Locate every uninfected red blood cell.
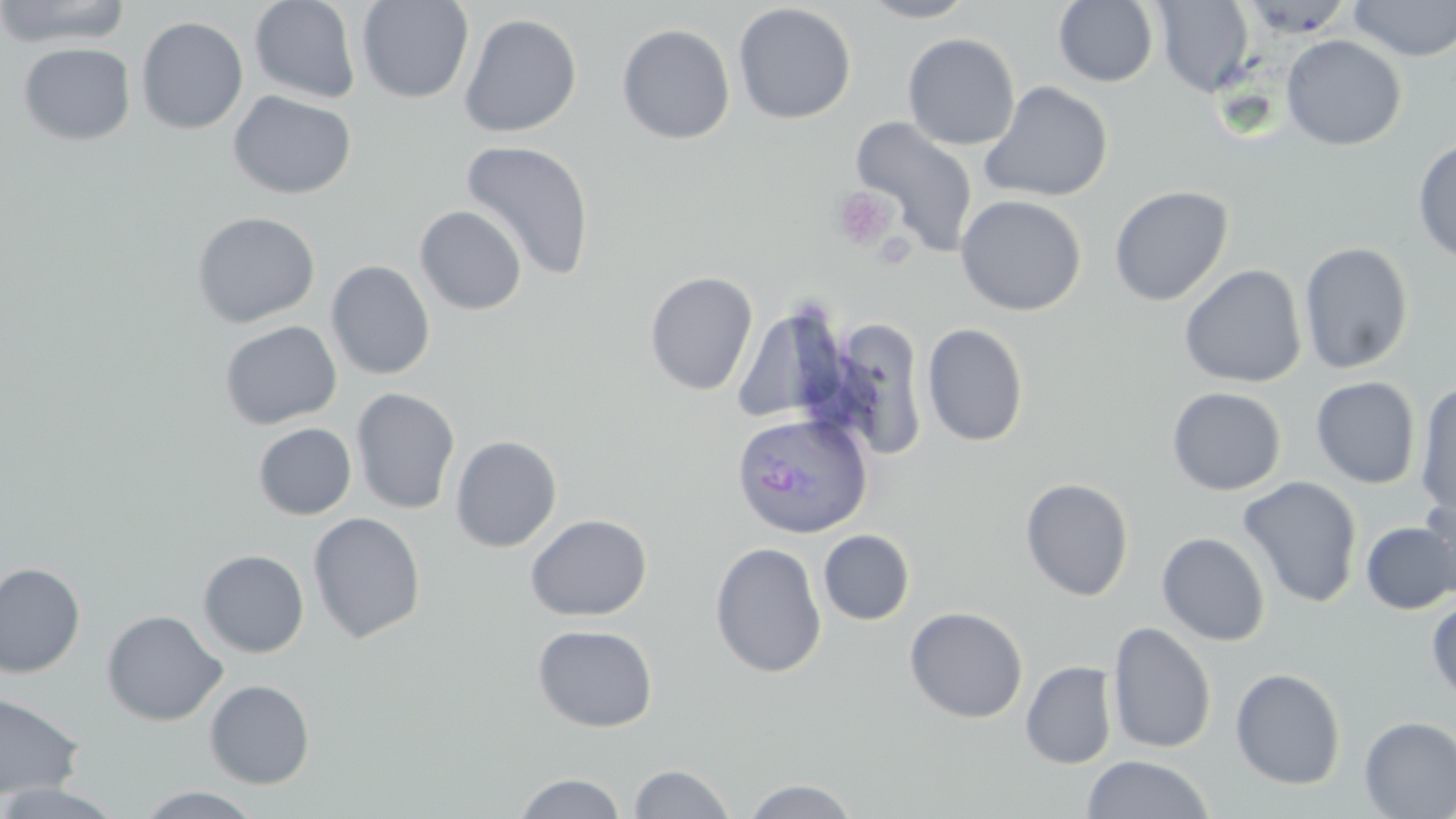
Approximate bounding boxes as named x1/y1/x2/y2 corners in pixels.
Uninfected red blood cells: (x1=0, y1=0, x2=133, y2=48), (x1=249, y1=0, x2=362, y2=104), (x1=356, y1=0, x2=474, y2=104), (x1=858, y1=0, x2=978, y2=23), (x1=1054, y1=0, x2=1159, y2=87), (x1=1348, y1=0, x2=1456, y2=61), (x1=1153, y1=1, x2=1255, y2=97), (x1=733, y1=3, x2=857, y2=124), (x1=458, y1=12, x2=582, y2=138), (x1=136, y1=16, x2=249, y2=135), (x1=616, y1=23, x2=735, y2=144), (x1=902, y1=33, x2=1020, y2=151), (x1=1281, y1=35, x2=1407, y2=151), (x1=18, y1=42, x2=136, y2=146), (x1=980, y1=80, x2=1114, y2=203), (x1=228, y1=90, x2=356, y2=200), (x1=849, y1=116, x2=979, y2=257), (x1=460, y1=139, x2=595, y2=282), (x1=1412, y1=139, x2=1456, y2=264), (x1=1109, y1=185, x2=1233, y2=306), (x1=955, y1=194, x2=1087, y2=316), (x1=414, y1=205, x2=527, y2=316), (x1=191, y1=211, x2=320, y2=328), (x1=1299, y1=242, x2=1414, y2=374), (x1=326, y1=260, x2=436, y2=380), (x1=1179, y1=264, x2=1307, y2=389), (x1=644, y1=271, x2=759, y2=396), (x1=731, y1=300, x2=851, y2=428), (x1=838, y1=316, x2=924, y2=459), (x1=219, y1=320, x2=342, y2=430), (x1=921, y1=322, x2=1029, y2=447), (x1=1311, y1=376, x2=1420, y2=489), (x1=1415, y1=382, x2=1456, y2=519), (x1=350, y1=387, x2=461, y2=515), (x1=1167, y1=387, x2=1286, y2=496), (x1=253, y1=422, x2=357, y2=519), (x1=450, y1=435, x2=562, y2=553), (x1=1238, y1=476, x2=1363, y2=607), (x1=1020, y1=477, x2=1134, y2=601), (x1=1419, y1=491, x2=1456, y2=600), (x1=308, y1=511, x2=426, y2=643), (x1=525, y1=514, x2=652, y2=621), (x1=1360, y1=522, x2=1456, y2=615), (x1=818, y1=529, x2=915, y2=625), (x1=1156, y1=532, x2=1271, y2=646), (x1=710, y1=541, x2=827, y2=679), (x1=197, y1=549, x2=309, y2=657), (x1=0, y1=562, x2=85, y2=678), (x1=1427, y1=598, x2=1456, y2=705), (x1=904, y1=606, x2=1028, y2=723), (x1=102, y1=610, x2=227, y2=725), (x1=1107, y1=621, x2=1217, y2=754), (x1=532, y1=624, x2=659, y2=733), (x1=1020, y1=661, x2=1118, y2=769), (x1=1230, y1=667, x2=1347, y2=790), (x1=204, y1=679, x2=315, y2=789), (x1=0, y1=693, x2=85, y2=799), (x1=1358, y1=716, x2=1456, y2=818), (x1=1081, y1=754, x2=1214, y2=819), (x1=627, y1=763, x2=737, y2=819), (x1=513, y1=772, x2=627, y2=818), (x1=741, y1=778, x2=861, y2=818), (x1=0, y1=782, x2=126, y2=818), (x1=133, y1=786, x2=266, y2=819).

Summary:
  - Platelet locations: (x1=831, y1=186, x2=897, y2=250)
  - Plasmodium ovale-infected red blood cell locations: (x1=730, y1=411, x2=873, y2=540)
  - Slide-level diagnosis: Plasmodium ovale
  - Magnification: 1000x
  - Modality: optical microscopy
  - Stain: May-Grünwald-Giemsa
  - Field of view: one of a larger specimen
  - Image size: 1456×819 pixels
  - Preparation: thin blood film